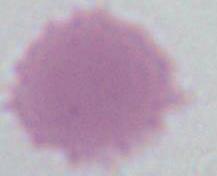

{
  "magnification": "1000x",
  "identification": "red blood cell",
  "modality": "photomicrograph"
}